Outline each Plasmodium falciparum-infected red blood cell.
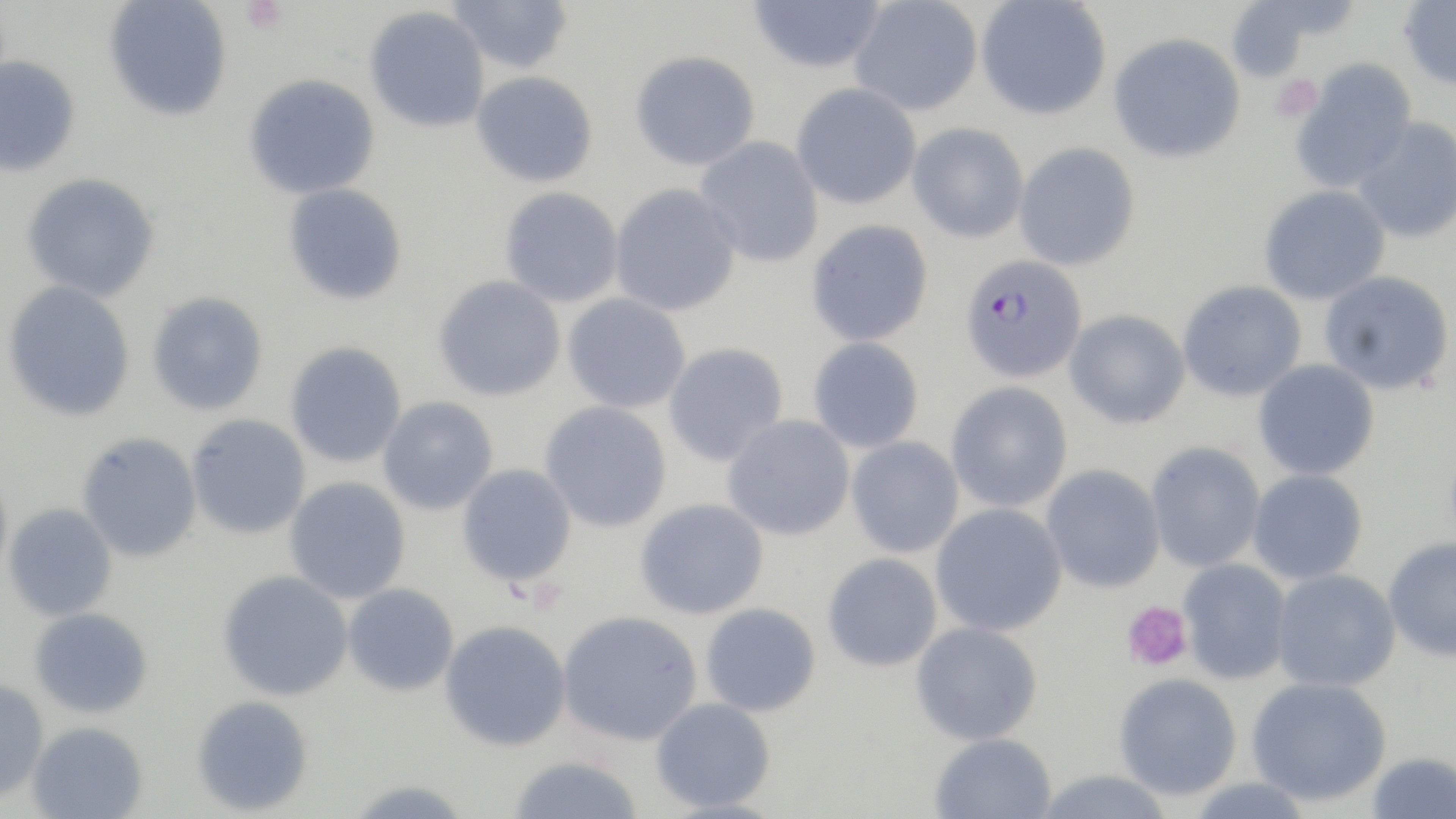
Approximate bounding boxes as named x1/y1/x2/y2 corners in pixels.
Plasmodium falciparum-infected red blood cells: (x1=958, y1=253, x2=1088, y2=383).

Summary:
  - Platelet locations: (x1=240, y1=0, x2=287, y2=35), (x1=1271, y1=75, x2=1321, y2=122), (x1=1121, y1=600, x2=1193, y2=672)
  - Uninfected red blood cell locations: (x1=103, y1=0, x2=232, y2=122), (x1=446, y1=0, x2=574, y2=74), (x1=747, y1=0, x2=887, y2=74), (x1=849, y1=0, x2=983, y2=117), (x1=975, y1=0, x2=1112, y2=120), (x1=1222, y1=0, x2=1343, y2=83), (x1=1399, y1=0, x2=1456, y2=92), (x1=364, y1=6, x2=490, y2=133), (x1=1108, y1=32, x2=1247, y2=164), (x1=629, y1=50, x2=761, y2=171), (x1=0, y1=55, x2=81, y2=178), (x1=1290, y1=57, x2=1417, y2=192), (x1=471, y1=70, x2=599, y2=188), (x1=243, y1=73, x2=380, y2=200), (x1=791, y1=83, x2=922, y2=210), (x1=1351, y1=117, x2=1456, y2=244), (x1=907, y1=123, x2=1028, y2=244), (x1=695, y1=136, x2=825, y2=268), (x1=1014, y1=142, x2=1141, y2=271), (x1=20, y1=173, x2=160, y2=302), (x1=282, y1=183, x2=408, y2=306), (x1=610, y1=183, x2=742, y2=317), (x1=1258, y1=184, x2=1391, y2=305), (x1=499, y1=187, x2=624, y2=308), (x1=806, y1=219, x2=933, y2=347), (x1=1318, y1=270, x2=1455, y2=396), (x1=432, y1=275, x2=567, y2=402), (x1=2, y1=280, x2=136, y2=422), (x1=1177, y1=280, x2=1308, y2=402), (x1=146, y1=291, x2=269, y2=416), (x1=562, y1=293, x2=691, y2=414), (x1=1064, y1=308, x2=1191, y2=429), (x1=808, y1=336, x2=924, y2=453), (x1=285, y1=341, x2=407, y2=468), (x1=663, y1=342, x2=789, y2=467), (x1=1253, y1=359, x2=1380, y2=480), (x1=945, y1=381, x2=1073, y2=513), (x1=378, y1=396, x2=499, y2=516), (x1=540, y1=401, x2=672, y2=533), (x1=186, y1=413, x2=312, y2=539), (x1=722, y1=414, x2=856, y2=541), (x1=76, y1=432, x2=203, y2=562), (x1=846, y1=436, x2=964, y2=558), (x1=1145, y1=441, x2=1266, y2=572), (x1=456, y1=463, x2=577, y2=587), (x1=0, y1=464, x2=13, y2=594), (x1=1041, y1=464, x2=1166, y2=593), (x1=1247, y1=469, x2=1368, y2=585), (x1=284, y1=476, x2=411, y2=604), (x1=634, y1=497, x2=770, y2=620), (x1=2, y1=503, x2=118, y2=621), (x1=930, y1=503, x2=1067, y2=637), (x1=1383, y1=537, x2=1456, y2=663), (x1=822, y1=552, x2=942, y2=672), (x1=1177, y1=557, x2=1292, y2=685), (x1=1271, y1=569, x2=1401, y2=693), (x1=217, y1=570, x2=353, y2=700), (x1=342, y1=583, x2=460, y2=697), (x1=700, y1=602, x2=821, y2=717), (x1=29, y1=607, x2=154, y2=719), (x1=557, y1=610, x2=703, y2=746), (x1=439, y1=620, x2=572, y2=751), (x1=911, y1=621, x2=1043, y2=746), (x1=1113, y1=674, x2=1242, y2=801), (x1=1246, y1=676, x2=1391, y2=807), (x1=0, y1=678, x2=49, y2=801), (x1=191, y1=695, x2=314, y2=816), (x1=650, y1=697, x2=776, y2=812), (x1=26, y1=721, x2=148, y2=818), (x1=930, y1=732, x2=1057, y2=819), (x1=1366, y1=751, x2=1455, y2=818), (x1=505, y1=755, x2=647, y2=818), (x1=1030, y1=769, x2=1176, y2=819), (x1=1182, y1=776, x2=1318, y2=818), (x1=342, y1=778, x2=474, y2=818)
  - Slide-level diagnosis: Plasmodium falciparum
  - Image size: 1456×819 pixels
  - Magnification: 1000x
  - Field of view: single
  - Stain: May-Grünwald-Giemsa
  - Modality: optical microscopy
  - Preparation: thin blood film